Outline each blood parasite and name the species.
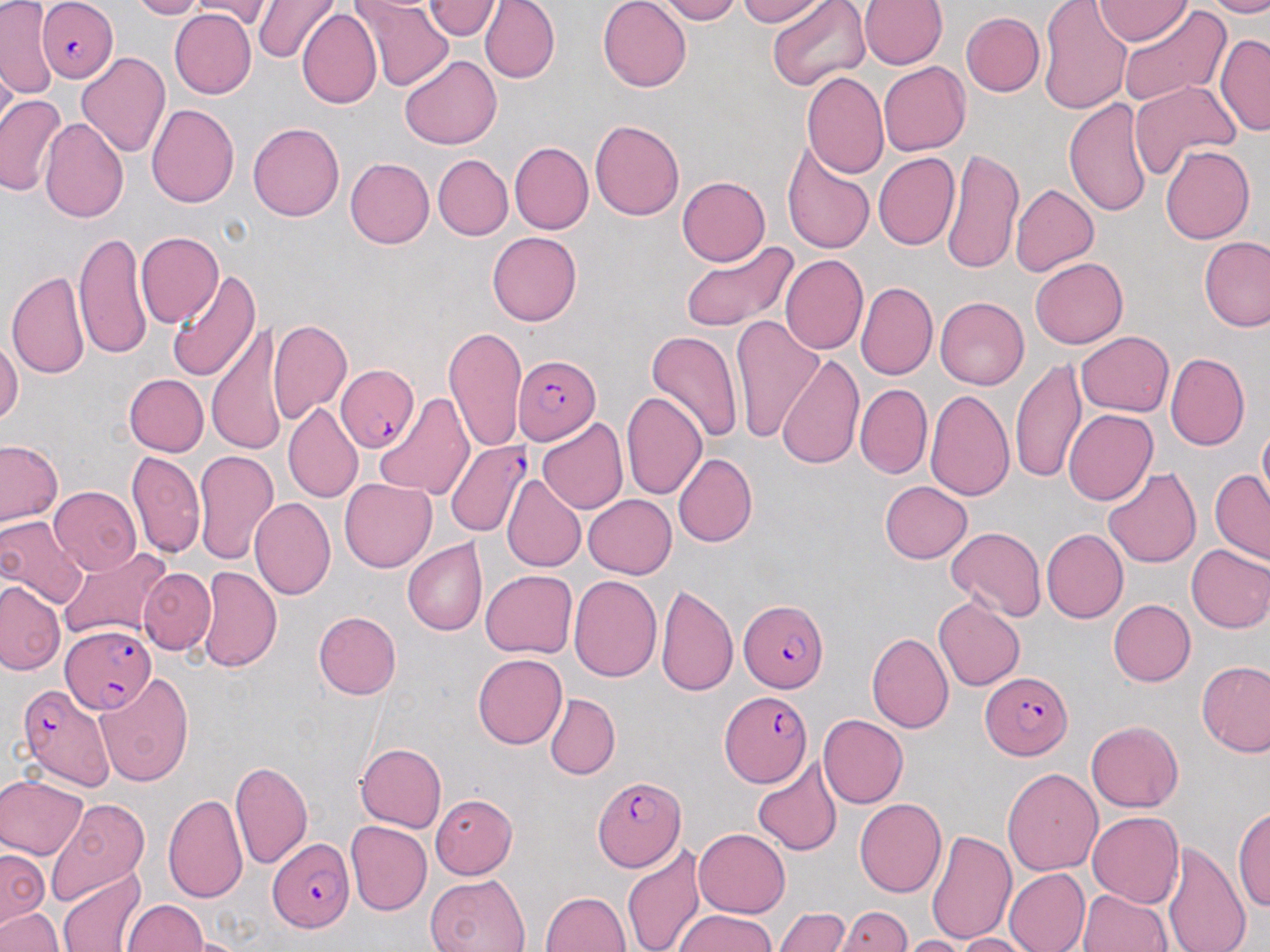
Approximate bounding boxes as (x1,y1)-(x2,y2) corner pairs in pixels.
Plasmodium falciparum-infected red blood cells (subset): (35,0)-(117,82), (515,354)-(600,446), (336,366)-(419,454), (446,442)-(527,537), (738,598)-(830,693), (60,625)-(161,710), (977,671)-(1070,758), (19,683)-(115,791), (591,773)-(687,874), (266,837)-(353,932).
No Plasmodium ovale, Plasmodium malariae, Plasmodium vivax, Babesia divergens, or Trypanosoma brucei observed.

Uninfected red blood cell locations (subset): (128,0)-(208,18), (185,0)-(276,25), (252,0)-(336,64), (427,0)-(501,40), (480,0)-(559,82), (597,0)-(691,91), (658,0)-(740,23), (735,0)-(826,25), (766,0)-(869,92), (860,0)-(947,70), (1038,0)-(1131,114), (1097,0)-(1187,45), (1209,0)-(1270,15), (359,2)-(454,91), (0,3)-(56,98), (1113,7)-(1229,110), (169,9)-(256,98), (298,9)-(383,112), (963,11)-(1044,97), (1215,33)-(1270,136), (76,51)-(172,158), (399,56)-(501,149), (880,64)-(970,155), (803,72)-(889,181), (1130,81)-(1239,177), (0,95)-(66,198), (1063,97)-(1153,216), (147,103)-(239,210), (41,117)-(130,225), (590,117)-(685,222), (247,121)-(343,223), (508,143)-(591,234), (1161,143)-(1258,243), (782,145)-(873,254), (941,150)-(1023,274), (872,152)-(960,251), (432,155)-(511,240), (343,157)-(434,249), (677,174)-(769,264), (1010,183)-(1098,279), (76,231)-(153,358), (136,232)-(223,329), (487,232)-(581,327), (1199,236)-(1270,333), (677,239)-(799,333), (781,255)-(868,355), (1030,258)-(1130,348), (168,267)-(259,381), (7,270)-(89,382), (857,280)-(937,380), (935,296)-(1031,389), (731,314)-(825,444), (208,320)-(289,457), (267,320)-(352,424), (444,324)-(529,455), (1077,330)-(1174,416), (647,332)-(739,442), (0,337)-(21,428), (1167,351)-(1250,451), (776,352)-(868,472), (1010,358)-(1087,484), (123,374)-(207,456), (857,385)-(932,478), (926,388)-(1013,500), (620,389)-(708,500), (374,395)-(474,499), (283,404)-(363,503), (1064,410)-(1158,507), (535,417)-(627,514), (1256,420)-(1269,499), (0,439)-(65,529), (193,448)-(278,564), (126,451)-(206,561), (675,452)-(758,548), (1102,465)-(1200,570), (1211,470)-(1269,563), (505,475)-(585,571), (340,478)-(436,569), (881,479)-(972,562), (49,485)-(142,575), (582,494)-(676,578), (249,497)-(337,602), (0,516)-(82,609), (946,523)-(1045,619), (1043,529)-(1128,622), (404,538)-(487,635), (1186,542)-(1270,633), (62,547)-(170,642), (197,566)-(283,672), (140,568)-(215,654), (481,570)-(577,659), (568,575)-(661,686), (0,576)-(67,678), (656,581)-(738,696), (933,595)-(1025,690), (1107,598)-(1195,686), (313,612)-(401,699), (869,630)-(953,733), (474,654)-(566,749), (1198,660)-(1270,757), (95,673)-(195,787), (545,694)-(618,778), (818,714)-(907,807), (1087,720)-(1184,810), (356,741)-(448,830), (753,758)-(840,855), (230,759)-(313,869), (1003,766)-(1103,876), (0,775)-(87,860), (165,792)-(251,905), (431,794)-(516,878), (45,795)-(152,906), (854,798)-(945,899), (1233,803)-(1269,915), (1087,809)-(1183,906), (345,821)-(431,915), (926,825)-(1017,944), (693,828)-(789,916), (1205,830)-(1263,952), (622,842)-(707,952), (1163,842)-(1248,952), (1,848)-(45,927), (1003,869)-(1092,952), (58,871)-(144,952), (424,873)-(530,952), (1077,888)-(1171,952), (540,889)-(632,952), (123,898)-(210,951), (840,906)-(914,951), (0,907)-(63,952), (775,907)-(850,952), (671,911)-(783,951), (951,930)-(1038,951), (900,934)-(976,952). Slide-level diagnosis: Plasmodium falciparum. Light microscopy. One field of a larger specimen. Thin blood smear. 1000x magnification. Image is 1270×952 pixels. May-Grünwald-Giemsa stain.